Point out each leukocyte.
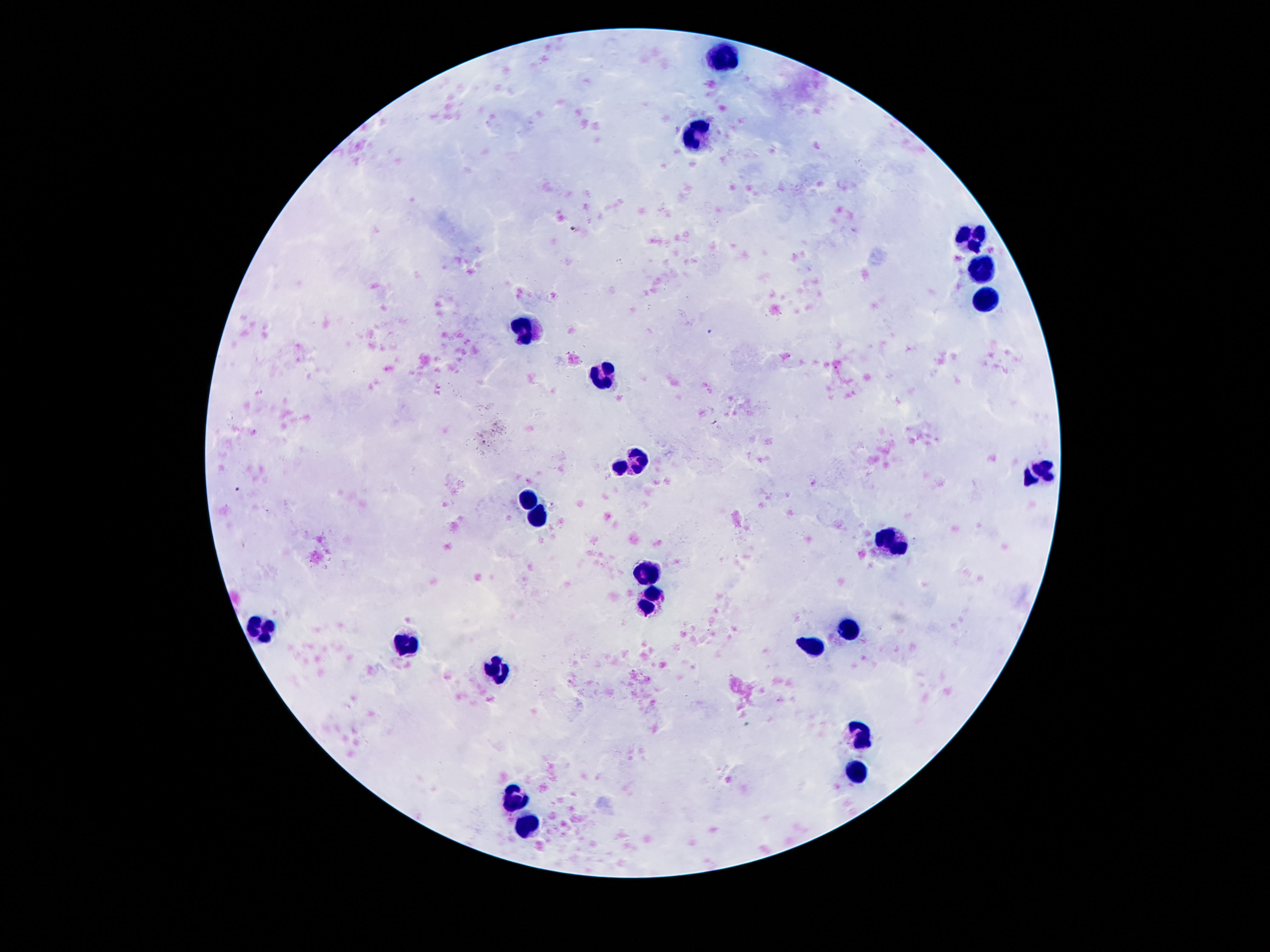
Approximate centers as [x, y] in pixels.
Leukocytes: [726, 57], [697, 133], [974, 238], [983, 270], [987, 300], [525, 325], [604, 373], [631, 458], [619, 467], [1045, 467], [1028, 479], [528, 498], [538, 518], [894, 544], [648, 575], [653, 597], [853, 627], [260, 629], [408, 644], [811, 646], [497, 671], [860, 732], [858, 774], [517, 796], [527, 824].

Giemsa-stained preparation. Thick blood smear. Single field of view. Image is 1270×952 pixels. Photographed through the microscope eyepiece with a smartphone camera. 100x magnification. Patient malaria status: uninfected.